Outline each blood parasite and name the species.
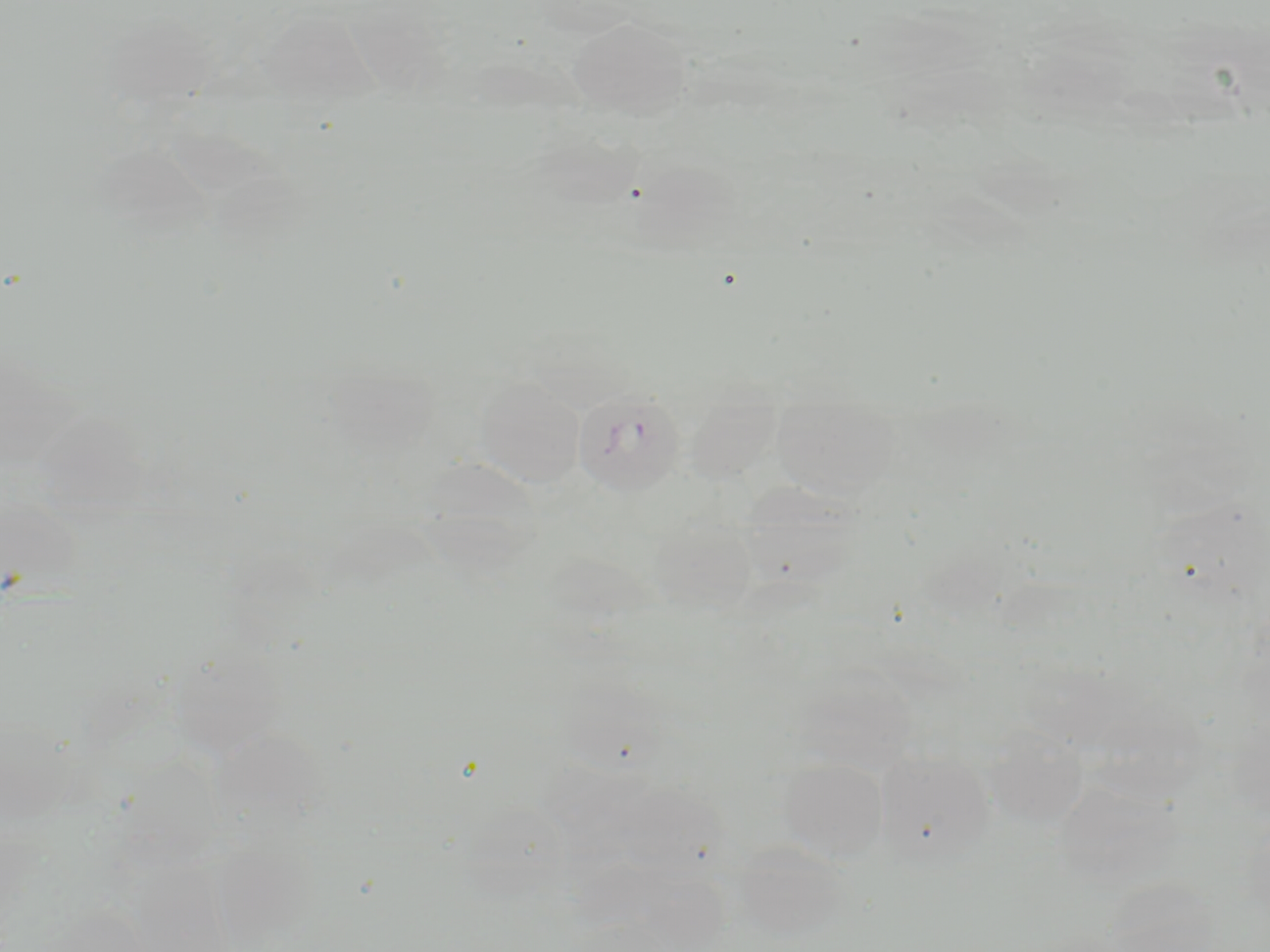
Approximate bounding boxes as (x1, y1, x2, y2) in pixels.
Plasmodium ovale-infected red blood cells: (572, 386, 686, 496).
No Plasmodium falciparum, Plasmodium malariae, Plasmodium vivax, Babesia divergens, or Trypanosoma brucei observed.

Uninfected red blood cell locations: (258, 10, 375, 107), (566, 17, 693, 118), (529, 331, 627, 406), (474, 375, 587, 487), (771, 394, 901, 500), (737, 481, 863, 588), (0, 490, 83, 595), (648, 515, 757, 616), (174, 662, 297, 759), (792, 669, 918, 774), (982, 725, 1089, 829), (873, 750, 996, 868), (779, 758, 888, 862), (452, 778, 584, 911), (734, 842, 855, 944). Slide-level diagnosis: Plasmodium ovale. Light microscopy. May-Grünwald-Giemsa stain. 1000x magnification. One field of a larger specimen. Image is 1270×952 pixels. Thin blood smear.